Classify this cell by malaria status.
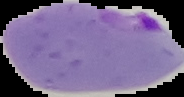
Parasitized.

From a thin blood smear. Image is 184×97 pixels. Segmented cell region on a black background.